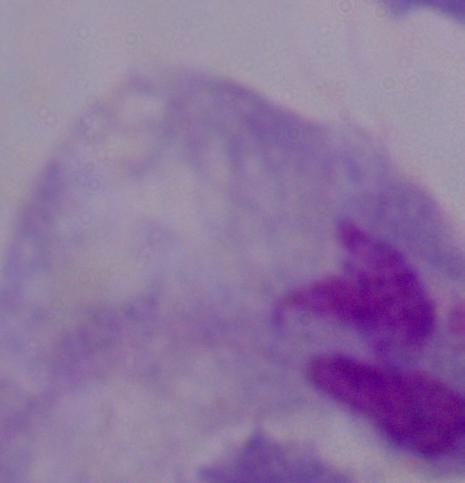
Summary:
  - Modality: micrograph
  - Magnification: 1000x
  - Identification: trichomonad